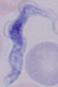
{
  "modality": "micrograph",
  "identification": "trypanosome",
  "magnification": "1000x"
}